Look for Plasmodium parasites.
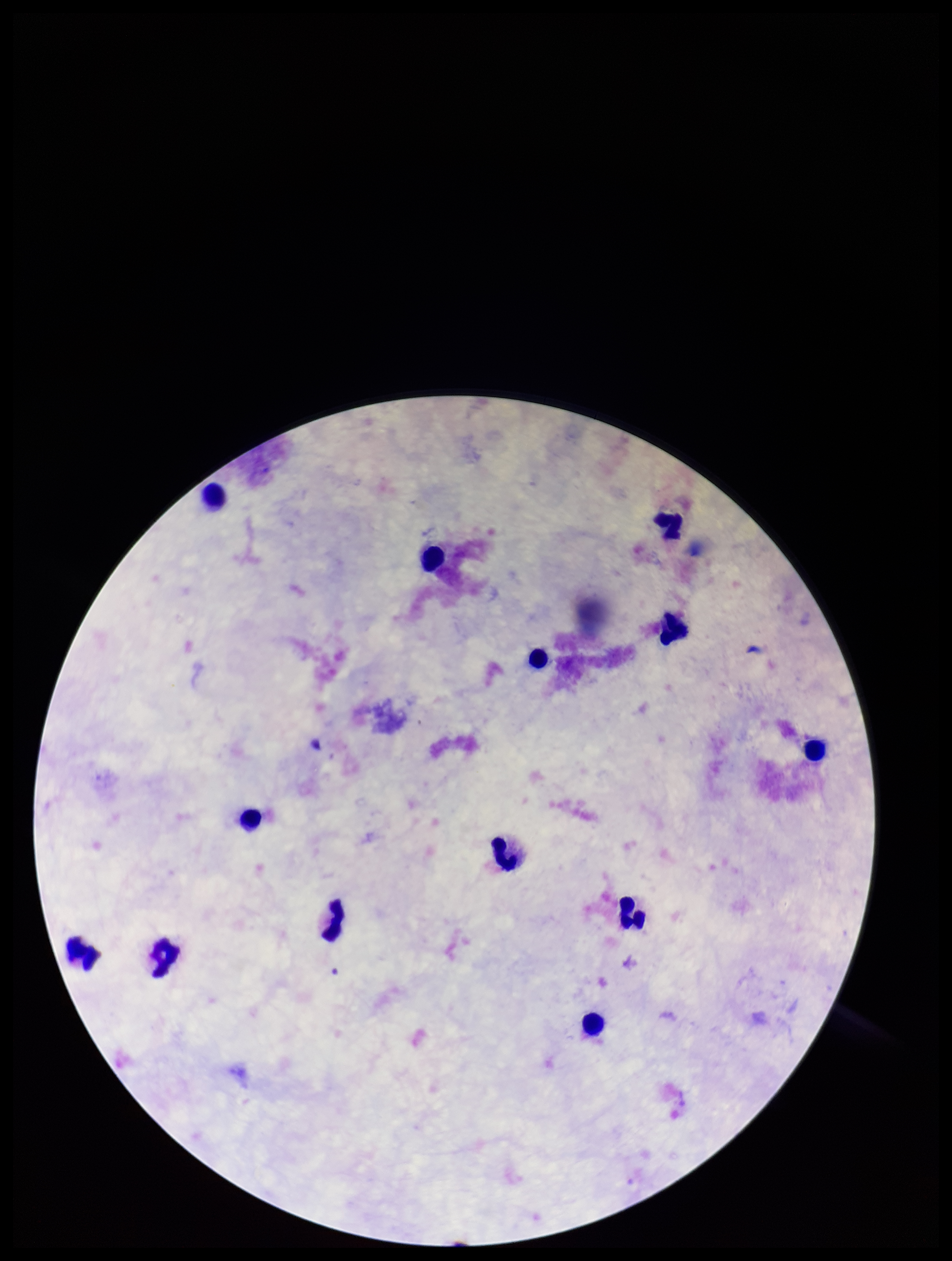
None seen.

stain = Giemsa
parasite count = 0
leukocyte count = 13
capture = smartphone photograph through the microscope eyepiece
preparation = thick blood smear
patient malaria status = negative
field of view = single
image size = 952×1261 pixels